Locate and identify every blood parasite.
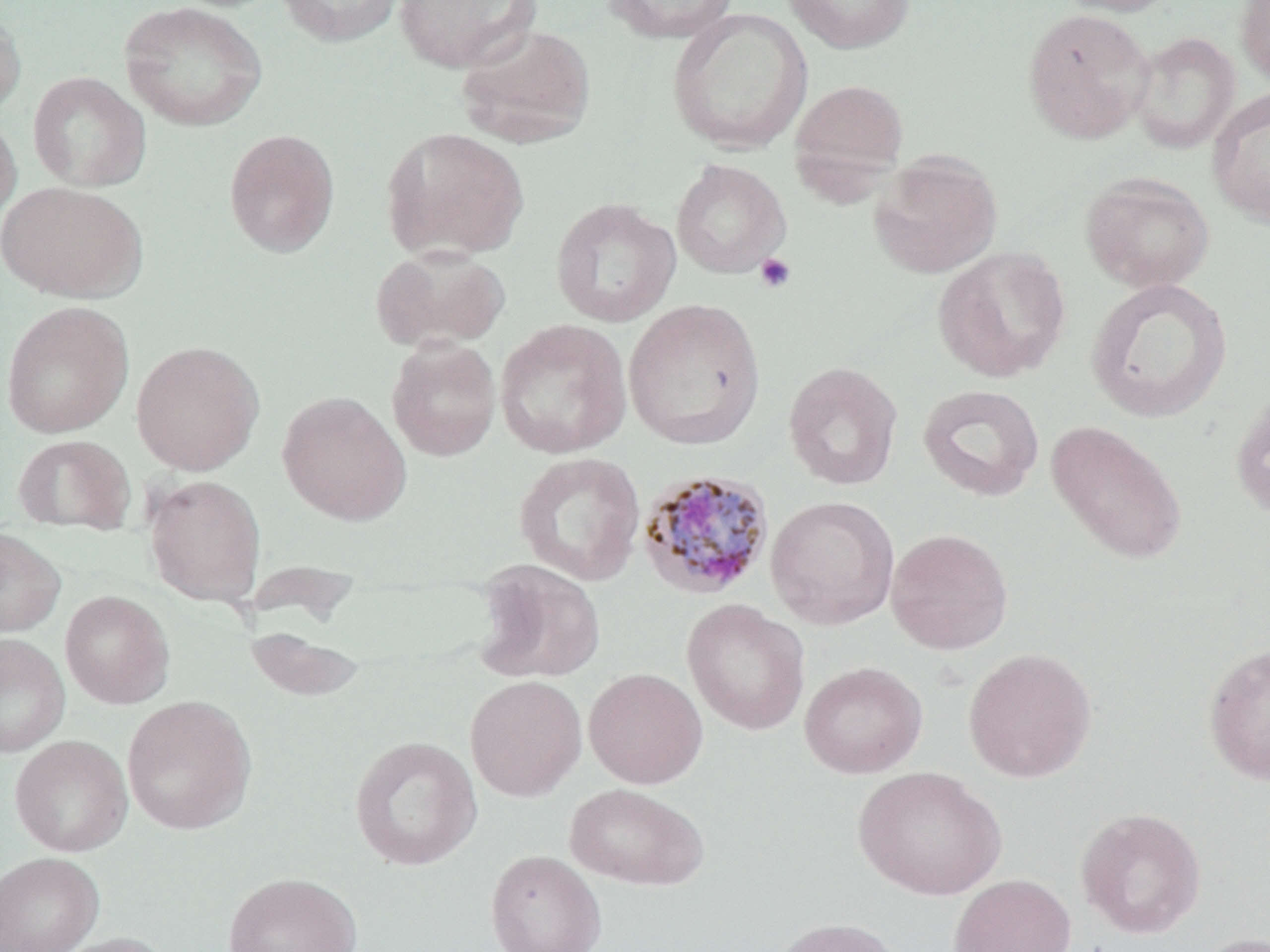
Approximate bounding boxes as (x1,y1)-(x2,y2) corner pairs in pixels.
Plasmodium malariae-infected red blood cells: (637,469)-(776,601).
No Plasmodium falciparum, Plasmodium ovale, Plasmodium vivax, Babesia divergens, or Trypanosoma brucei observed.

Summary:
  - Platelet locations: (754,253)-(796,293)
  - Uninfected red blood cell locations: (274,0)-(405,47), (393,0)-(541,73), (601,0)-(739,44), (782,0)-(915,54), (1052,0)-(1185,17), (1234,0)-(1270,88), (119,2)-(268,132), (0,5)-(26,121), (667,8)-(812,153), (1021,8)-(1156,144), (455,24)-(597,149), (1129,31)-(1241,155), (28,71)-(152,192), (788,78)-(909,192), (1206,86)-(1270,227), (0,111)-(21,231), (381,126)-(530,262), (223,127)-(340,258), (869,151)-(1003,279), (670,159)-(791,279), (1079,171)-(1214,293), (0,180)-(148,302), (550,197)-(681,328), (370,245)-(511,352), (932,246)-(1071,383), (1085,277)-(1233,423), (622,299)-(766,450), (1,301)-(134,438), (494,319)-(632,459), (386,338)-(502,461), (131,340)-(265,476), (783,361)-(903,490), (918,384)-(1045,502), (276,391)-(411,525), (1229,392)-(1270,520), (1045,420)-(1188,566), (12,434)-(135,536), (513,452)-(645,586), (144,474)-(266,606), (765,495)-(899,629), (0,526)-(67,638), (885,528)-(1013,654), (473,559)-(605,684), (60,590)-(175,709), (682,599)-(810,736), (245,626)-(368,703), (0,633)-(70,757), (1203,641)-(1270,785), (962,647)-(1098,783), (798,662)-(928,778), (583,668)-(708,789), (465,675)-(587,802), (121,695)-(257,835), (10,735)-(133,857), (348,735)-(483,872), (852,765)-(1006,900), (565,783)-(710,890), (1075,806)-(1207,939), (485,849)-(606,952), (0,851)-(103,952), (222,871)-(364,952), (947,873)-(1076,952), (770,917)-(905,952), (47,932)-(175,952), (1191,932)-(1270,952)
  - Slide-level diagnosis: Plasmodium malariae
  - Stain: May-Grünwald-Giemsa
  - Preparation: thin blood film
  - Image size: 1270×952 pixels
  - Field of view: single
  - Modality: optical microscopy
  - Magnification: 1000x